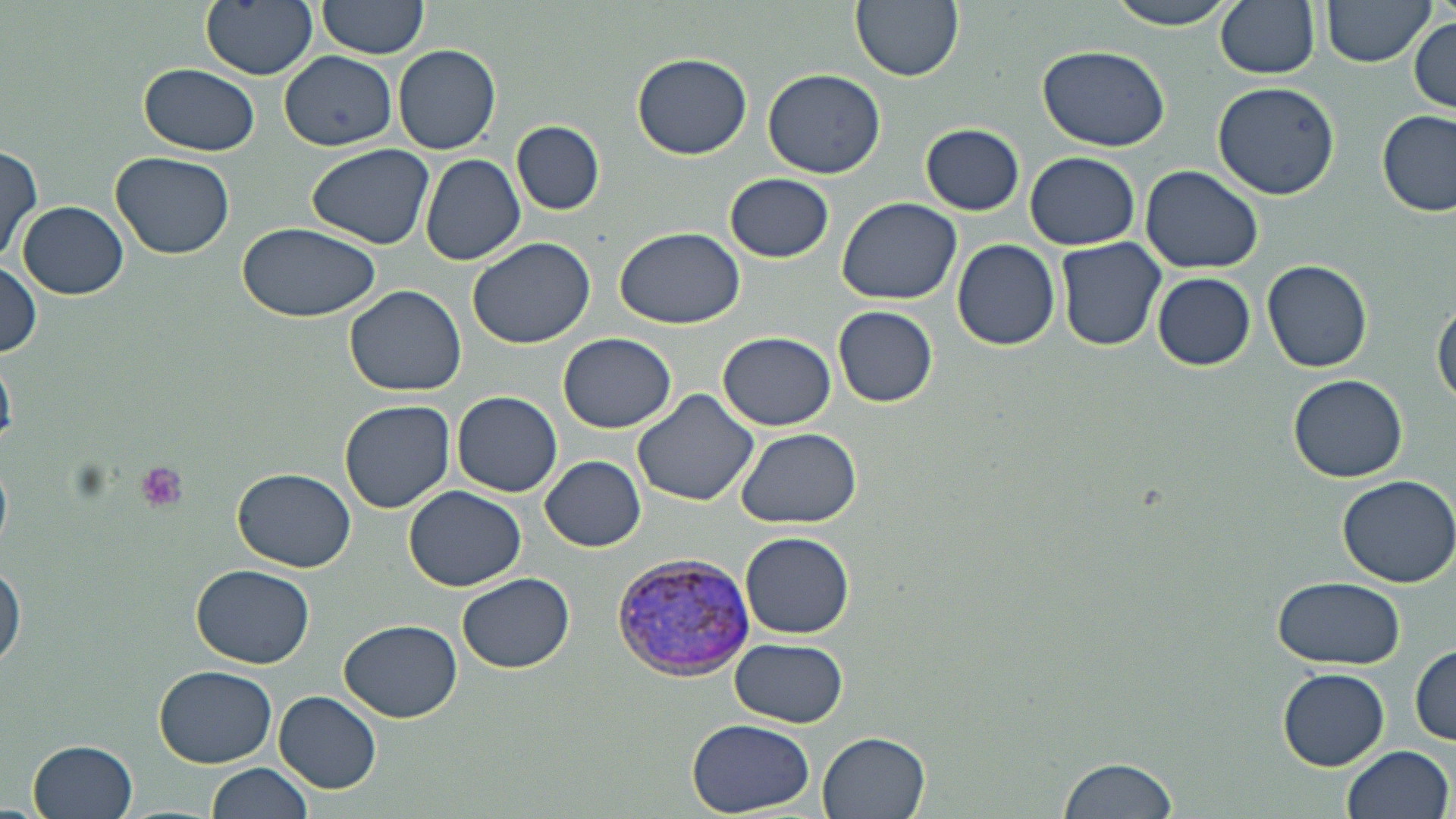

Plasmodium vivax-infected red blood cell locations = approximate bounding boxes as (x1,y1)-(x2,y2) corner pairs in pixels: (608,549)-(764,683)
slide-level diagnosis = Plasmodium vivax
preparation = thin blood film
image size = 1456×819 pixels
platelet locations = approximate bounding boxes as (x1,y1)-(x2,y2) corner pairs in pixels: (134,462)-(188,512)
uninfected red blood cell locations = approximate bounding boxes as (x1,y1)-(x2,y2) corner pairs in pixels: (201,0)-(318,78), (850,0)-(963,82), (1107,0)-(1239,30), (1215,0)-(1321,78), (1320,0)-(1435,66), (316,1)-(429,62), (1408,14)-(1456,114), (393,43)-(501,155), (1037,43)-(1170,152), (279,51)-(398,151), (631,51)-(753,161), (138,63)-(259,156), (763,68)-(885,179), (1212,79)-(1344,202), (1379,109)-(1454,217), (512,121)-(604,214), (920,122)-(1026,215), (306,143)-(435,250), (1,145)-(43,263), (111,150)-(236,258), (420,152)-(526,265), (1026,152)-(1140,249), (1140,165)-(1265,274), (724,172)-(834,262), (837,197)-(966,306), (19,201)-(128,300), (237,223)-(381,322), (615,225)-(748,328), (468,237)-(597,349), (1055,237)-(1168,351), (952,239)-(1061,349), (1262,257)-(1372,373), (0,264)-(43,360), (1152,273)-(1256,371), (345,285)-(468,397), (1432,298)-(1456,410), (833,305)-(939,408), (558,332)-(675,433), (718,332)-(836,431), (1287,373)-(1408,483), (632,388)-(762,509), (451,391)-(563,497), (339,399)-(456,514), (733,427)-(861,528), (540,455)-(647,552), (233,469)-(356,571), (1336,473)-(1455,588), (404,486)-(529,593), (739,532)-(854,638), (0,557)-(24,672), (192,564)-(314,670), (458,573)-(574,673), (1272,575)-(1406,669), (338,618)-(462,723), (713,634)-(842,813), (729,638)-(847,728), (1411,643)-(1455,745), (154,665)-(277,766), (1278,670)-(1389,769), (273,689)-(382,793), (687,718)-(816,815), (818,733)-(931,819), (28,739)-(139,819), (1339,745)-(1453,819), (1057,754)-(1180,819), (206,761)-(315,819)
stain = May-Grünwald-Giemsa
modality = light microscopy
magnification = 1000x
field of view = single